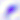

Summary:
  - Identification: Toxoplasma gondii
  - Magnification: 400x
  - Modality: photomicrograph